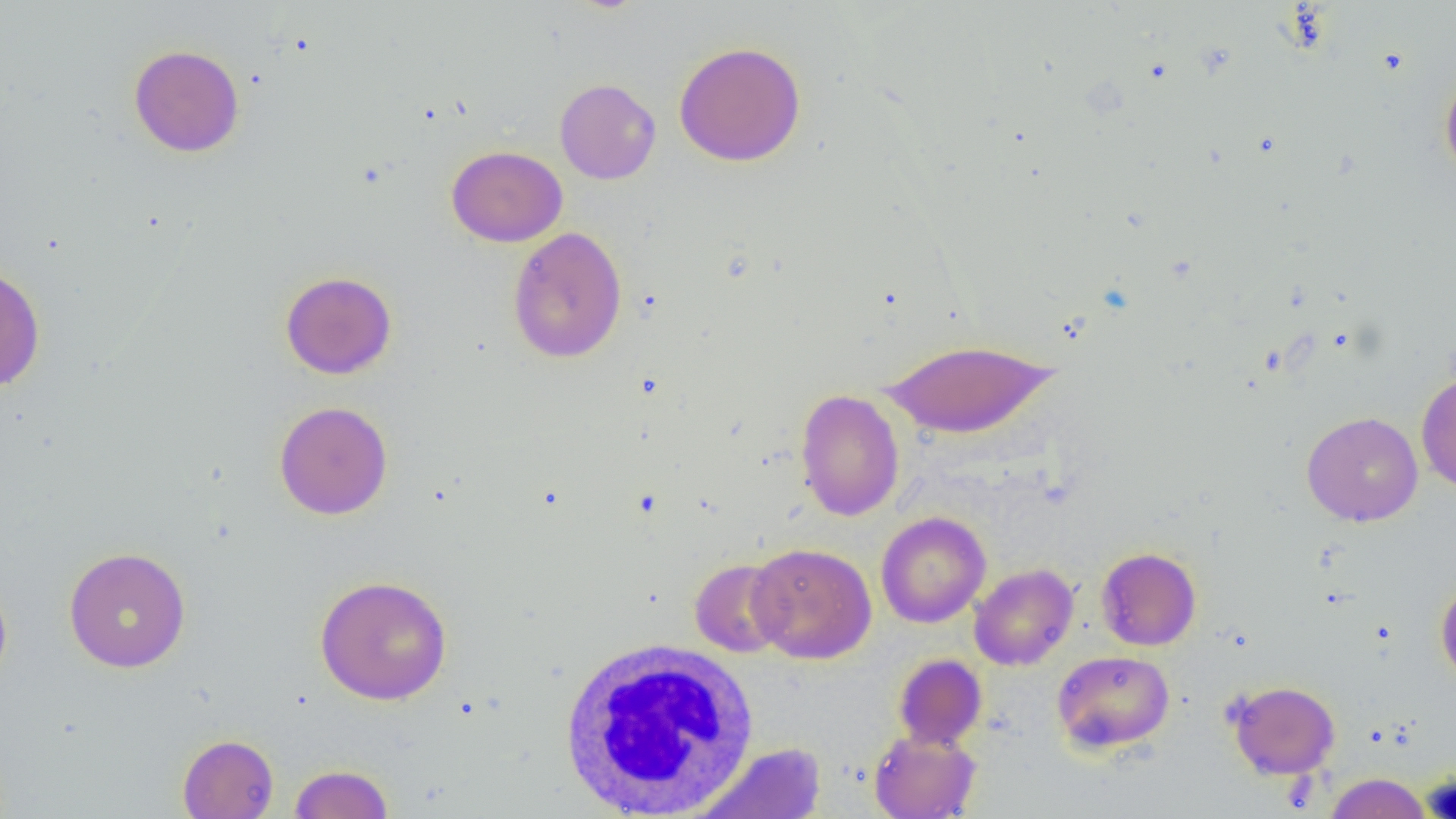
slide-level diagnosis = negative for blood parasites
uninfected red blood cell locations = approximate bounding boxes as named x1/y1/x2/y2 corners in pixels: (x1=674, y1=41, x2=806, y2=167), (x1=128, y1=44, x2=244, y2=157), (x1=1439, y1=66, x2=1456, y2=184), (x1=555, y1=78, x2=661, y2=184), (x1=446, y1=145, x2=567, y2=247), (x1=507, y1=226, x2=627, y2=364), (x1=0, y1=262, x2=46, y2=392), (x1=280, y1=271, x2=397, y2=379), (x1=881, y1=338, x2=1059, y2=439), (x1=1416, y1=371, x2=1456, y2=493), (x1=794, y1=388, x2=904, y2=521), (x1=274, y1=401, x2=393, y2=520), (x1=1301, y1=411, x2=1423, y2=526), (x1=876, y1=511, x2=991, y2=628), (x1=748, y1=541, x2=877, y2=664), (x1=63, y1=546, x2=191, y2=673), (x1=1096, y1=546, x2=1202, y2=651), (x1=689, y1=558, x2=790, y2=658), (x1=969, y1=563, x2=1079, y2=671), (x1=314, y1=574, x2=453, y2=705), (x1=0, y1=575, x2=13, y2=694), (x1=1435, y1=578, x2=1456, y2=689), (x1=1052, y1=650, x2=1175, y2=754), (x1=893, y1=654, x2=987, y2=749), (x1=1226, y1=680, x2=1340, y2=779), (x1=869, y1=728, x2=981, y2=819), (x1=177, y1=733, x2=279, y2=818), (x1=690, y1=742, x2=828, y2=819), (x1=289, y1=764, x2=394, y2=818), (x1=1323, y1=773, x2=1432, y2=818)
white blood cell locations = approximate bounding boxes as named x1/y1/x2/y2 corners in pixels: (x1=555, y1=636, x2=762, y2=816)
modality = optical microscopy
field of view = single
image size = 1456×819 pixels
preparation = thin blood film
magnification = 1000x